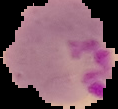

Image is 118×109 pixels. Segmented cell region on a black background. From a thin blood film. Result: Plasmodium parasites identified.